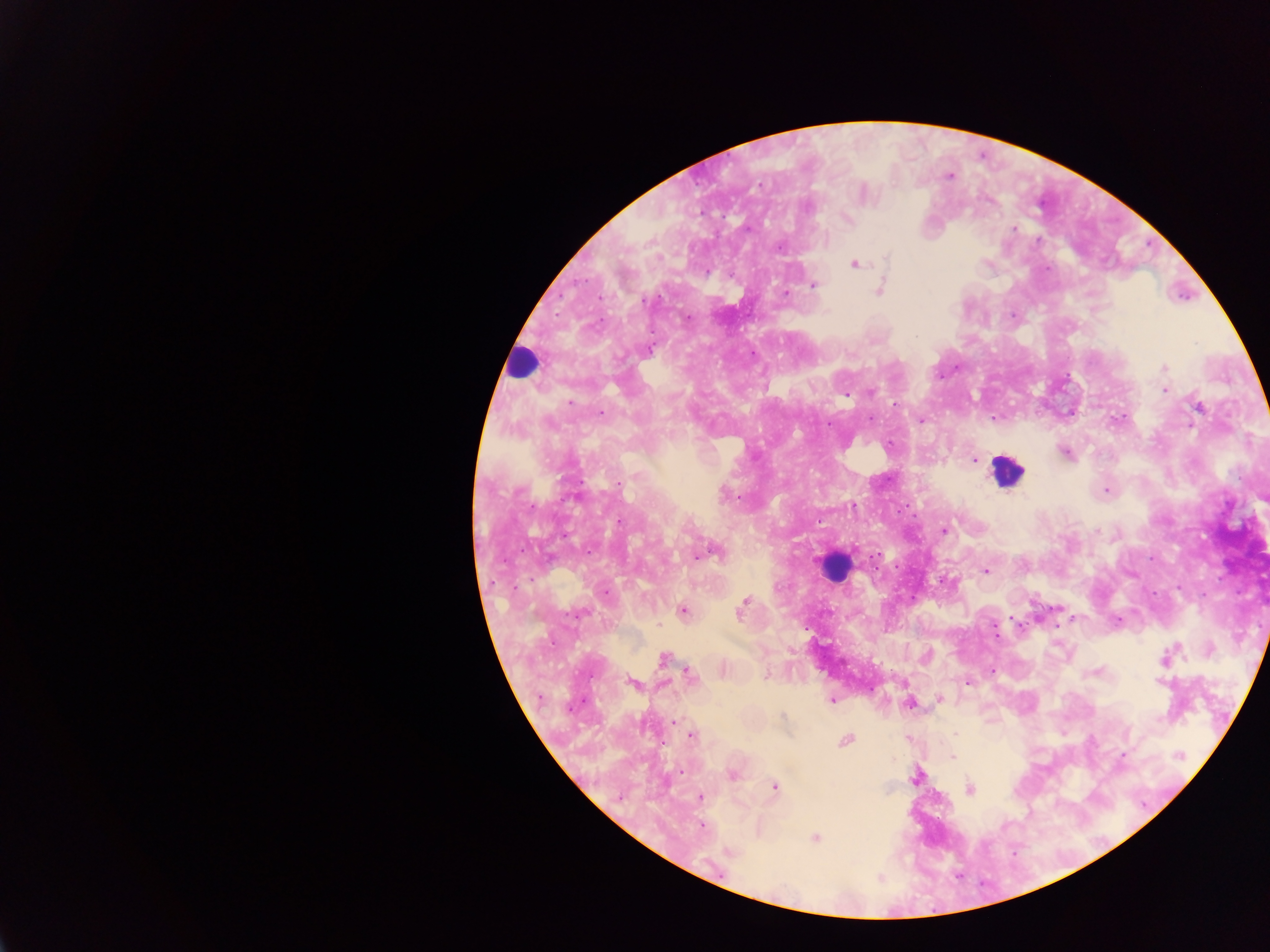
Approximate centers as (x, y) in pixels. Plasmodium parasite locations: (950, 176), (759, 184), (807, 207), (847, 219), (1015, 229), (1038, 240), (779, 247), (887, 258), (854, 264), (708, 272), (814, 286), (879, 290), (785, 294), (644, 301), (688, 318), (649, 350), (1164, 367), (1164, 390), (871, 393), (846, 394), (570, 403), (1198, 407), (601, 413), (871, 418), (993, 418), (921, 420), (1065, 453), (974, 459), (619, 484), (1106, 491), (724, 496), (852, 506), (619, 522), (943, 531), (715, 552), (985, 571), (605, 593), (741, 608), (683, 611), (579, 613), (1117, 620), (927, 656), (664, 658), (1165, 660), (689, 674), (632, 683), (968, 683), (939, 699), (831, 701), (909, 704), (783, 715), (675, 722), (955, 734), (691, 735), (845, 741), (1124, 754), (1179, 755), (952, 756), (682, 770), (733, 775), (916, 778), (775, 786), (969, 789), (700, 797), (701, 826), (815, 838), (730, 851). Leukocyte locations: (523, 362), (1005, 470), (833, 566). Image is 1270×952 pixels. Thick blood smear. Sample from Ghana. Photographed through a microscope with a mobile-phone camera. Single field of view.